Assess this cell for malaria.
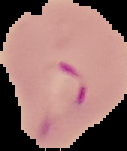

Parasitized.

Summary:
  - Image type: segmented cell region on a black background
  - Image size: 127×151 pixels
  - Preparation: thin blood film